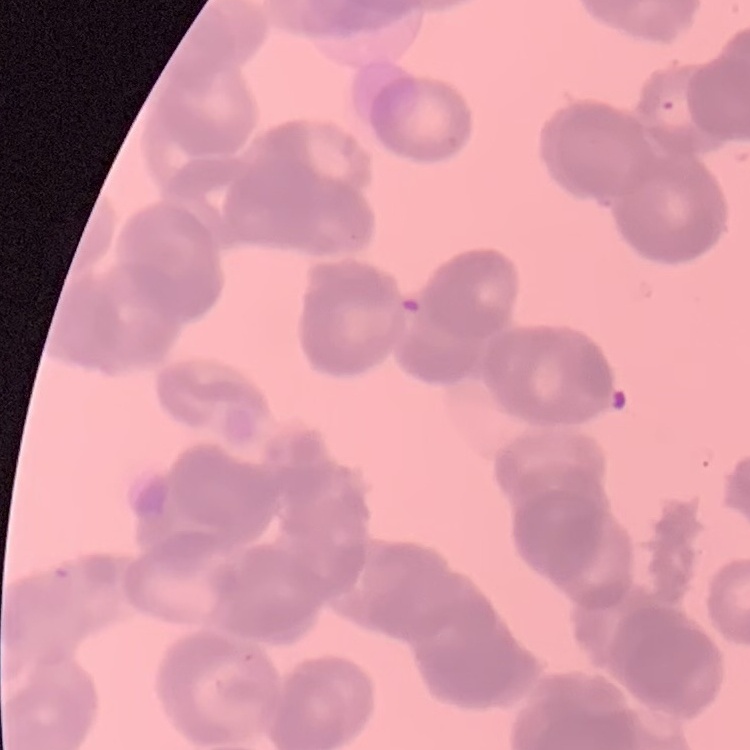

red blood cell morphology = rouleaux formation
preparation = thin blood smear
stain = Field's or Giemsa
image type = one tile cut from a larger photomicrograph